Assess this cell for malaria.
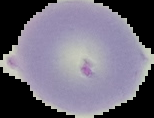

It is uninfected.

Summary:
  - Image type: cell region segmented out of the field of view; surrounding area masked to black
  - Image size: 154×118 pixels
  - Preparation: thin blood film